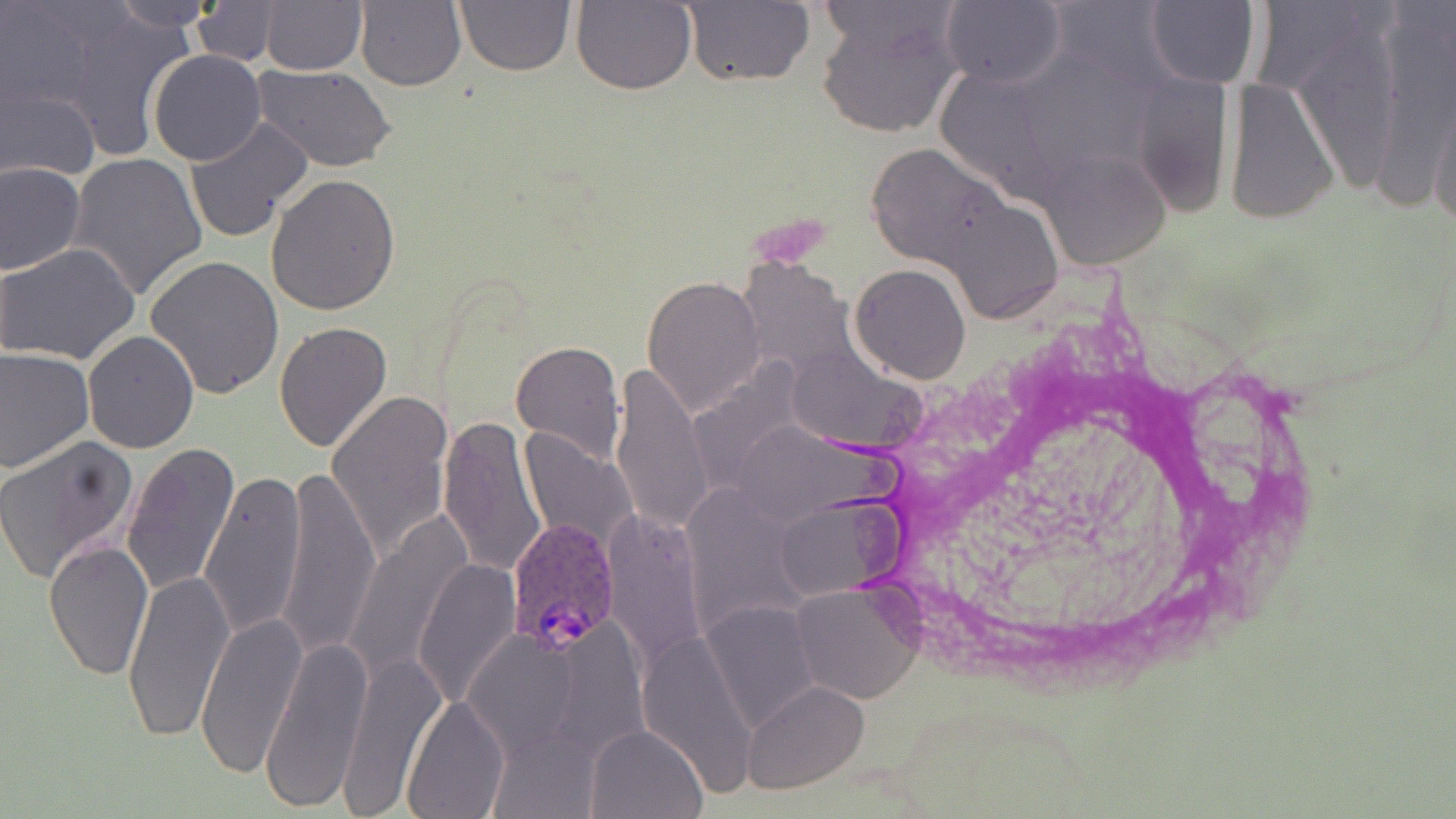

slide-level diagnosis = Plasmodium ovale
image size = 1456×819 pixels
magnification = 1000x
Plasmodium ovale-infected red blood cell locations = approximate bounding boxes as (x1,y1)-(x2,y2) corner pairs in pixels: (508,518)-(625,654)
field of view = one of a larger specimen
modality = light microscopy
stain = May-Grünwald-Giemsa
uninfected red blood cell locations = approximate bounding boxes as (x1,y1)-(x2,y2) corner pairs in pixels: (105,0)-(223,31), (258,0)-(366,75), (454,0)-(576,77), (187,1)-(285,66), (354,1)-(468,92), (569,1)-(697,94), (682,1)-(815,88), (940,1)-(1066,88), (1144,1)-(1260,89), (816,3)-(961,140), (148,50)-(267,166), (252,64)-(395,172), (0,76)-(101,185), (1226,77)-(1339,225), (1429,88)-(1456,237), (185,118)-(313,243), (863,139)-(1023,284), (69,152)-(207,301), (1040,152)-(1176,273), (1,161)-(84,276), (266,172)-(400,315), (0,243)-(141,367), (145,255)-(285,400), (850,263)-(972,384), (642,275)-(765,415), (273,321)-(392,453), (82,329)-(199,453), (511,341)-(626,464), (0,347)-(94,472), (610,367)-(714,541), (327,389)-(454,558), (438,412)-(547,579), (520,430)-(636,552), (0,434)-(139,582), (120,443)-(241,596), (275,465)-(382,657), (198,469)-(306,638), (772,495)-(908,602), (600,511)-(713,668), (345,517)-(469,685), (43,540)-(154,679), (411,558)-(524,710), (122,570)-(233,743), (788,582)-(923,704), (704,602)-(823,729), (195,614)-(304,777), (262,637)-(370,812), (342,652)-(445,808), (742,680)-(870,793), (401,696)-(510,819), (586,723)-(708,818)
preparation = thin blood smear